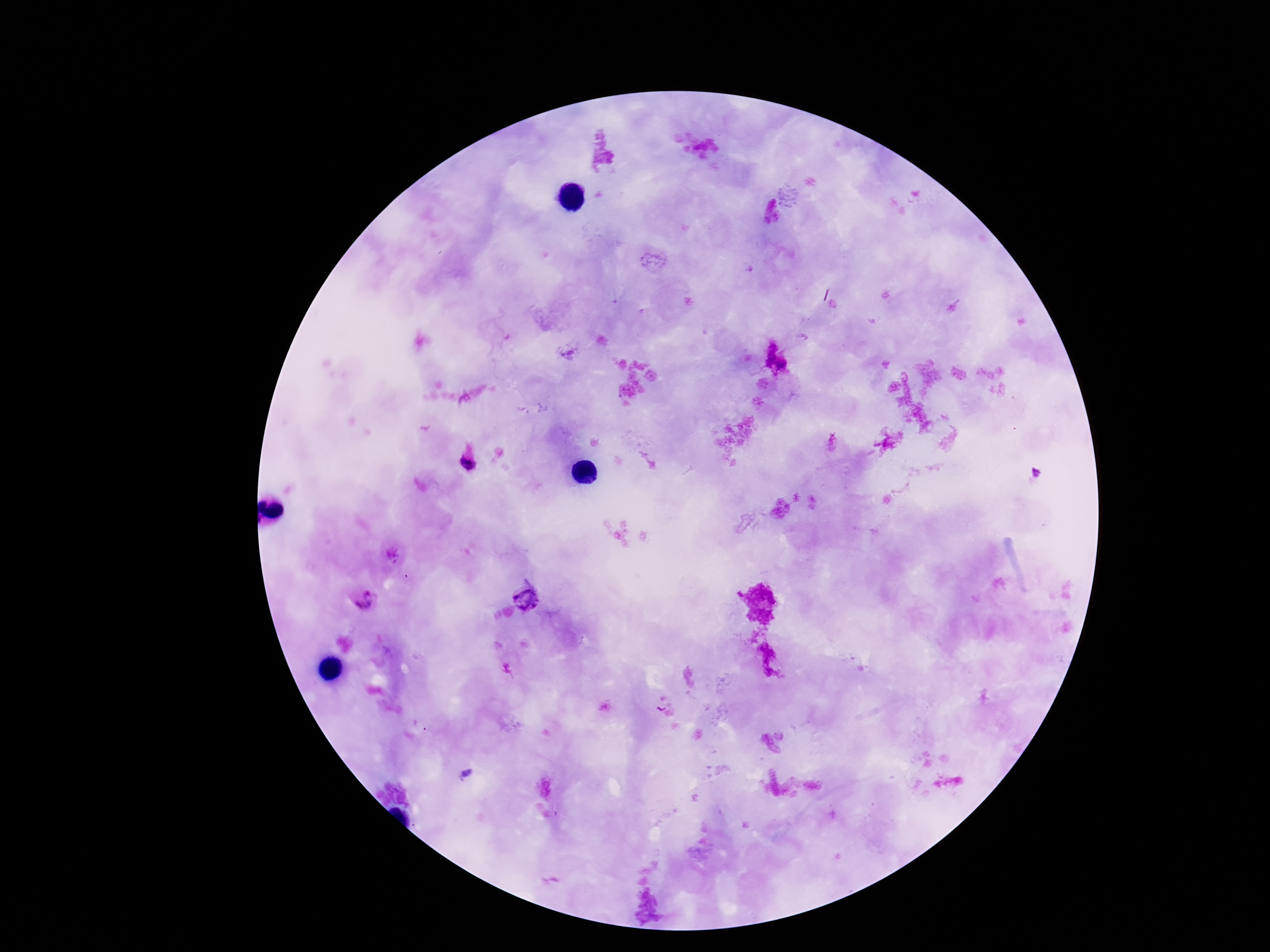
patient malaria status = infected
field of view = single
capture = smartphone camera through the microscope eyepiece
Plasmodium parasite locations = approximate centers as [x, y] in pixels: [465, 461], [528, 598], [366, 602]
magnification = 100x
image size = 1270×952 pixels
stain = Giemsa
preparation = thick blood film